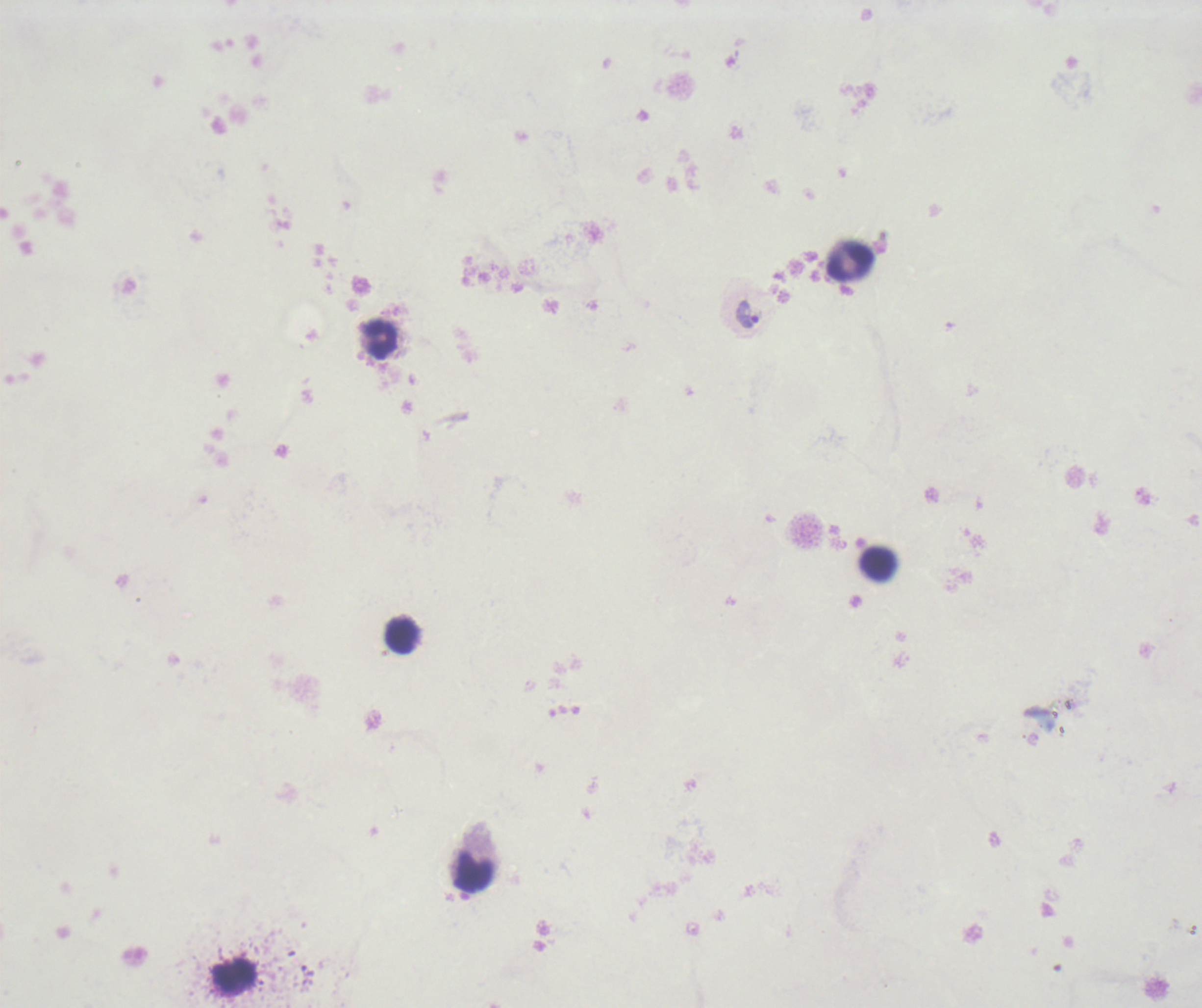

coordinate format = approximate centers as [x, y] in pixels
trophozoite locations = [746, 315]
leukocyte locations = [850, 262], [380, 338], [879, 565], [402, 635], [474, 873], [234, 977]
field of view = one from this slide
magnification = 100x
result = Plasmodium parasites identified
image size = 1202×1008 pixels
background quality = poor
stain = Romanowsky
coloration quality = bad
preparation = thick smear of blood
context = previously used in a real diagnosis